Give the position of every malaria parasite.
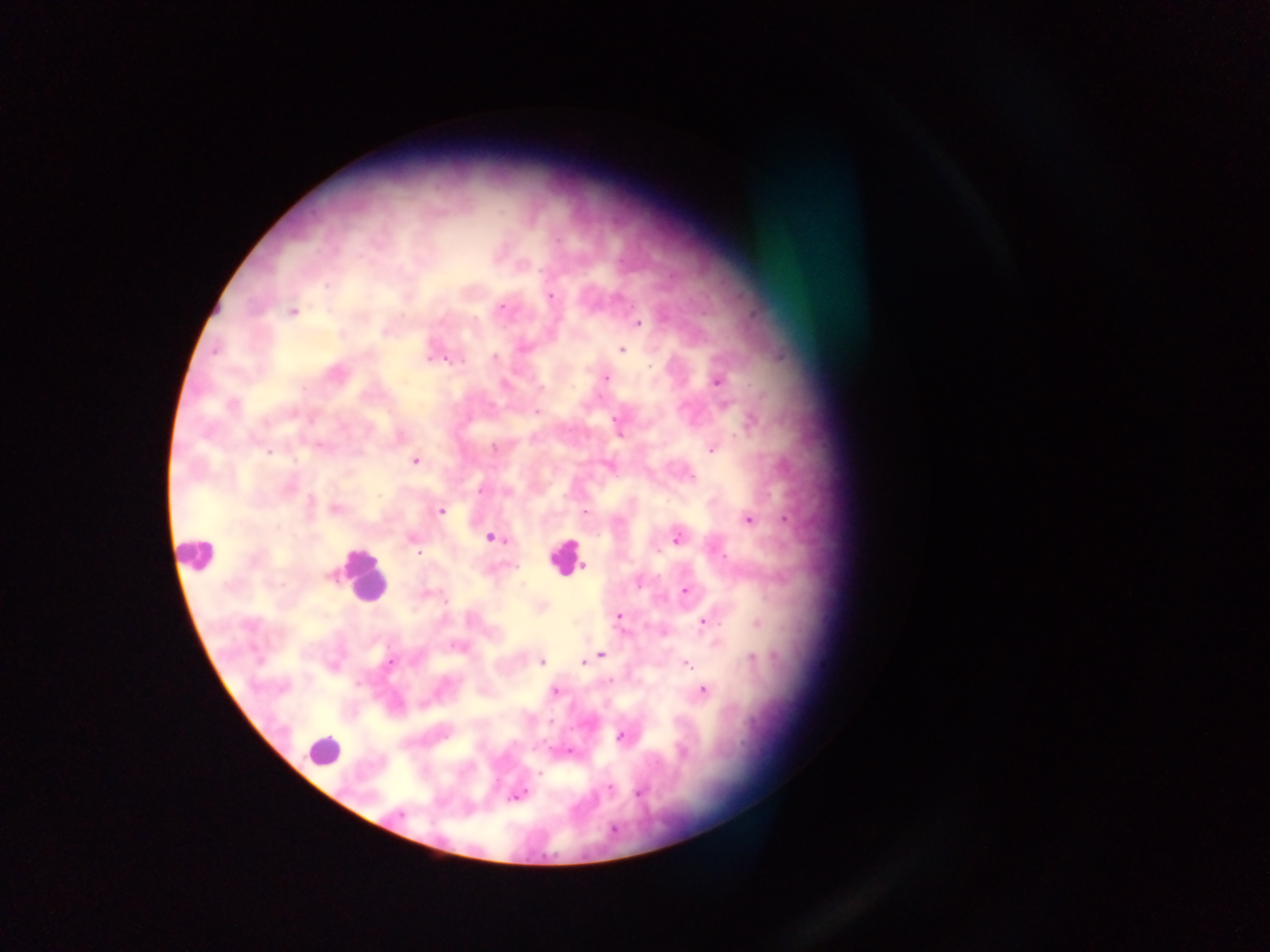

Approximate centers as (x, y) in pixels.
Malaria parasites: (328, 285), (551, 295), (503, 308), (292, 312), (639, 323), (384, 332), (523, 349), (216, 350), (622, 350), (430, 357), (495, 358), (453, 359), (460, 360), (606, 377), (718, 382), (232, 404), (538, 412), (617, 420), (752, 420), (320, 446), (493, 448), (711, 450), (269, 452), (415, 460), (691, 477), (480, 491), (310, 502), (335, 508), (440, 510), (585, 512), (749, 519), (785, 520), (412, 538), (491, 538), (677, 538), (418, 553), (584, 566), (685, 591), (445, 602), (618, 616), (705, 621), (601, 654), (751, 658), (593, 659), (541, 662), (583, 662), (390, 663), (688, 665), (610, 680), (702, 691), (555, 692), (550, 721), (620, 736), (569, 752), (684, 753), (539, 773), (609, 787), (638, 793), (517, 795), (399, 814).

{
  "capture": "mobile-phone photograph through a microscope",
  "field_of_view": "single",
  "leukocyte_locations": "approximate centers as (x, y) in pixels: (197, 554), (565, 556), (361, 577), (323, 750)",
  "preparation": "thick blood film",
  "image_size": "1270×952 pixels",
  "country": "Ghana"
}